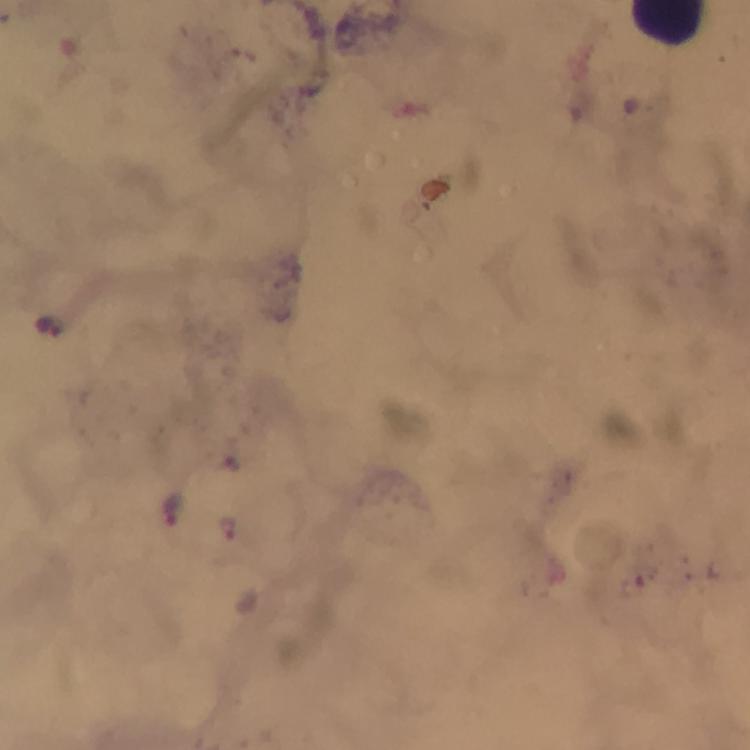
{
  "cropped_from": "one field of view",
  "preparation": "thick blood smear",
  "capture": "smartphone mounted on the microscope",
  "malaria_parasite_locations": "approximate centers as [x, y] in pixels: [50, 326], [175, 507], [229, 529]",
  "magnification": "100x",
  "immersion_oil": "used",
  "context": "from a diagnostic examination for malaria",
  "image_size": "750×750 pixels",
  "stain": "Giemsa"
}